Identify the parasite.
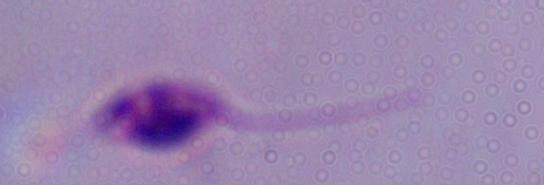
Leishmania.

Micrograph. Captured at 1000x magnification.